Assess this cell for malaria.
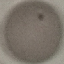
Uninfected.

Giemsa stain. Thin blood smear. Acquired by smartphone through the microscope eyepiece. Automatically extracted cell patch, resized to 64 × 64 pixels.